Classify this cell by malaria status.
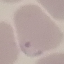

Parasitized.

Summary:
  - Capture: smartphone through the microscope eyepiece
  - Preparation: thin smear
  - Image type: automatically extracted cell patch, resized to 64 × 64 pixels
  - Stain: Giemsa